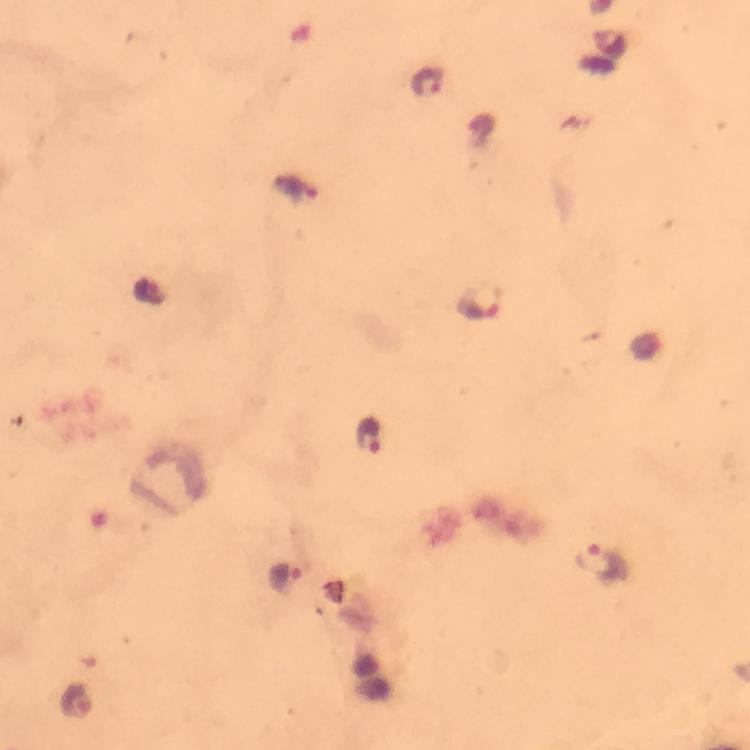

Approximate centers as (x, y) in pixels. Plasmodium parasite locations: (427, 80), (294, 189), (481, 302), (370, 436), (604, 565), (285, 576), (78, 700). A crop from one field of view. From a diagnostic examination for malaria. Photographed with a smartphone mounted on the microscope. Thick blood film. Giemsa stain. At 100x magnification. Image is 750×750 pixels. Immersion oil was used.